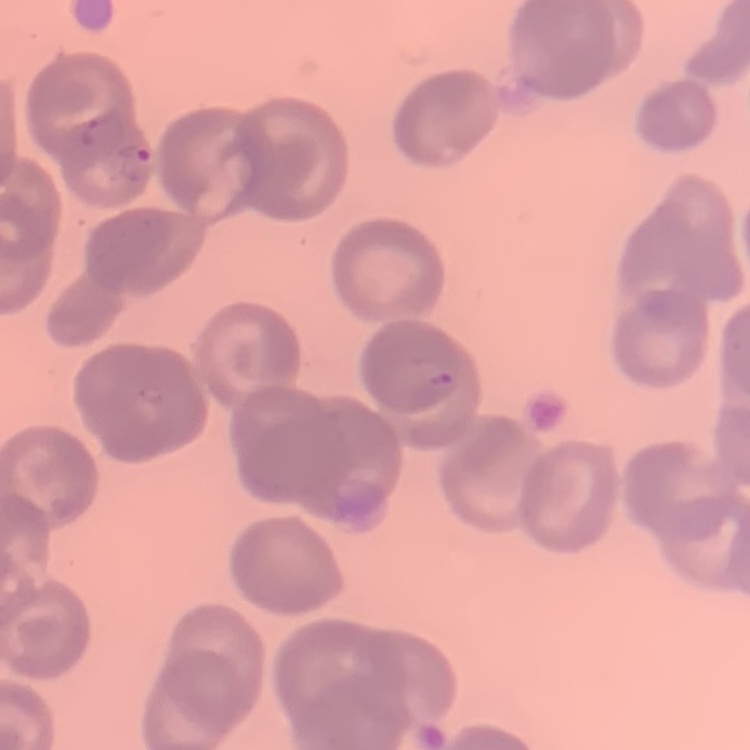
Summary:
  - Red blood cell morphology: no rouleaux formation
  - Image type: one tile cut from a larger photomicrograph
  - Preparation: thin peripheral smear
  - Stain: Field's or Giemsa